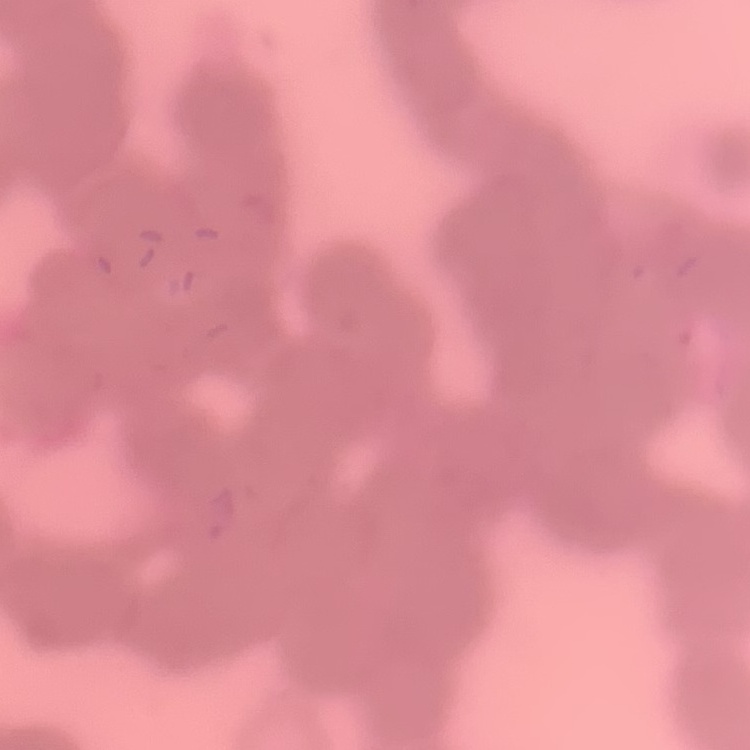 The red blood cells show rouleaux formation. One tile cut from a larger photomicrograph. Thin peripheral smear. Stained with either Field's or Giemsa.